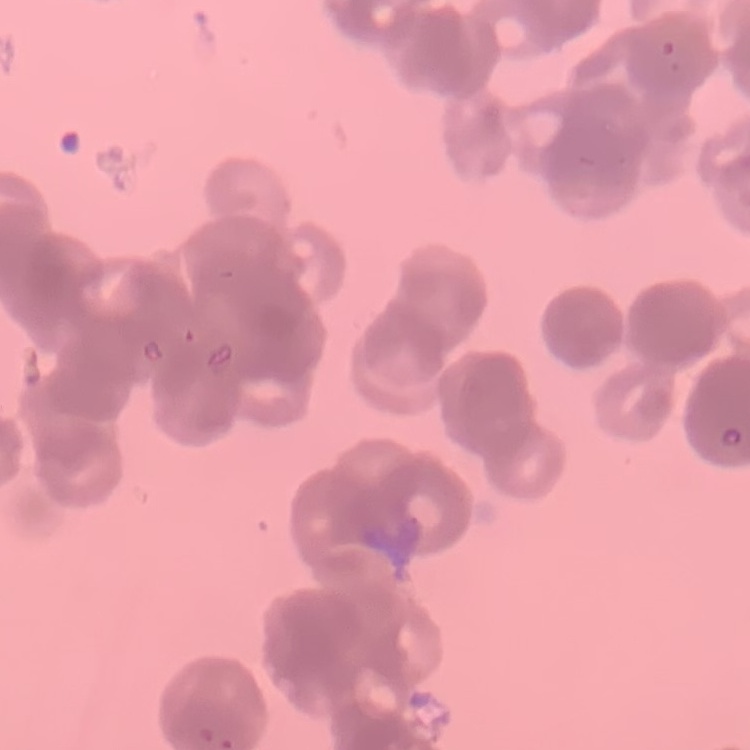
erythrocyte_morphology: rouleaux formation
preparation: thin blood film
image_type: square crop of a larger photomicrograph
stain: Field's or Giemsa